Locate every leukocyte (white blood cell).
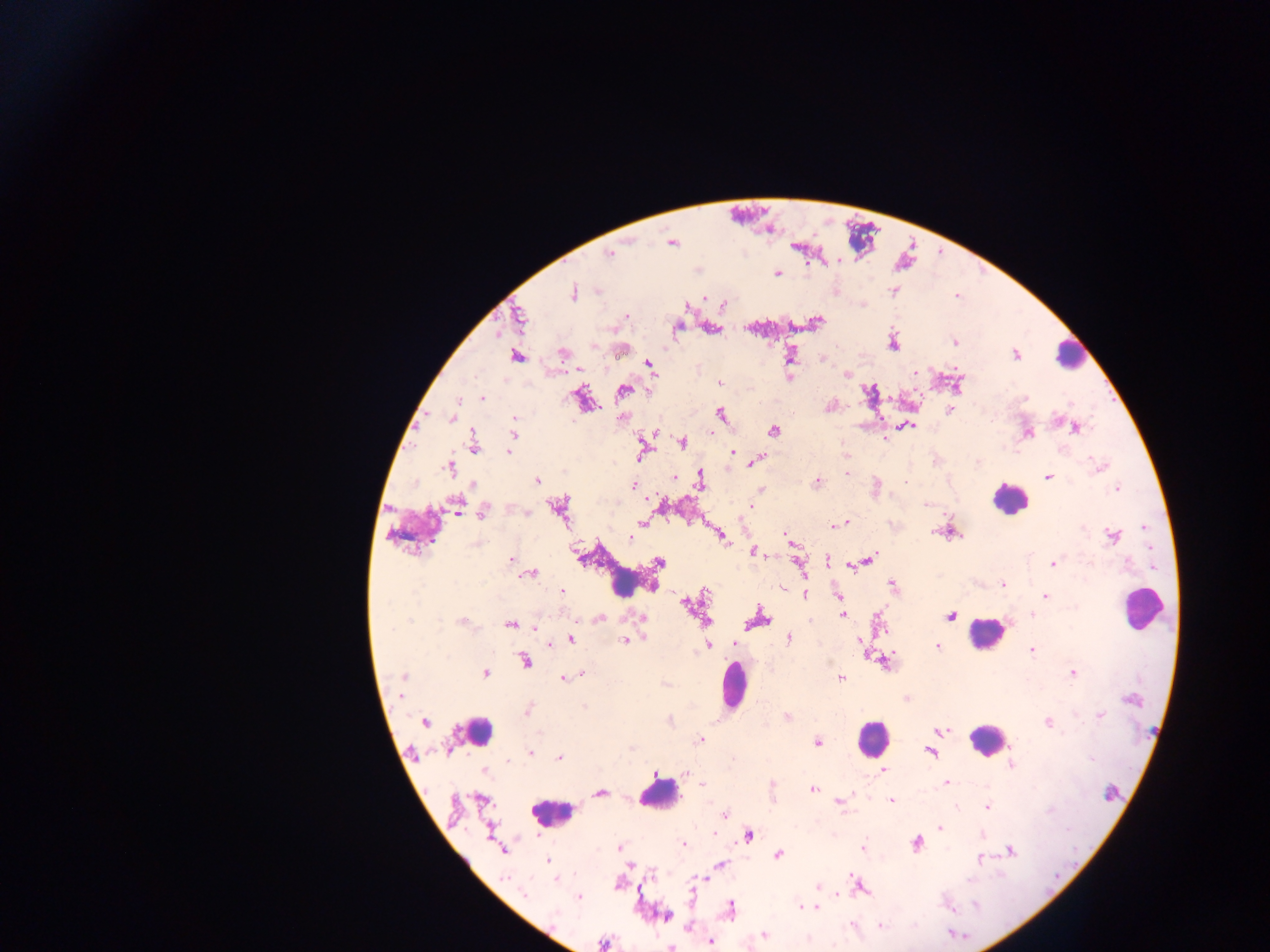

Approximate centers as x y in pixels.
Leukocytes: 1070 354; 1010 500; 632 579; 1143 609; 986 633; 732 685; 476 730; 872 738; 987 740; 658 792; 550 813.

Summary:
  - Malaria parasite locations: 671 242; 609 254; 777 274; 894 290; 572 292; 704 297; 724 304; 625 315; 518 317; 816 322; 711 328; 892 342; 954 342; 619 350; 561 353; 789 354; 1016 354; 516 356; 648 362; 577 368; 845 373; 788 376; 720 383; 957 384; 622 390; 482 398; 1025 398; 581 399; 830 406; 949 409; 721 414; 453 417; 514 417; 621 417; 904 426; 1075 427; 774 429; 1027 432; 514 433; 885 439; 682 442; 474 444; 641 449; 508 451; 732 452; 756 460; 1099 466; 449 467; 846 472; 673 477; 1047 477; 536 480; 699 480; 817 482; 633 486; 876 487; 1116 487; 760 490; 751 505; 456 506; 559 508; 483 511; 642 522; 844 522; 838 524; 832 525; 950 531; 719 535; 1112 535; 630 536; 787 537; 753 551; 511 559; 869 559; 827 560; 658 561; 797 561; 1053 564; 849 566; 529 573; 1002 583; 892 586; 782 590; 561 591; 704 592; 804 593; 838 596; 1045 596; 688 604; 1031 614; 843 615; 949 615; 599 618; 642 618; 878 618; 757 619; 462 622; 511 624; 535 626; 571 639; 624 639; 788 639; 861 639; 550 643; 733 643; 707 645; 937 645; 1032 649; 523 660; 885 661; 1073 672; 485 673; 582 673; 402 677; 563 678; 839 678; 907 698; 527 709; 1100 715; 788 717; 425 721; 1048 722; 942 731; 699 740; 816 742; 930 750; 531 752; 559 757; 1011 765; 884 770; 686 773; 947 783; 702 784; 812 787; 1110 792; 599 793; 892 800; 839 801; 987 806; 725 815; 940 828; 747 835; 683 843; 917 844; 619 847; 862 849; 503 850; 1009 850; 778 854; 980 859; 548 860; 630 864; 720 864; 556 878; 703 878; 857 884; 818 887; 523 894; 578 897; 800 906; 815 907; 807 908; 731 909; 666 916; 764 934; 710 941; 603 943; 669 946
  - Image size: 1270×952 pixels
  - Field of view: single
  - Capture: mobile-phone photograph through a microscope
  - Country: Ghana
  - Preparation: thick blood film